Assess this cell for malaria.
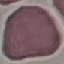

It is uninfected.

{
  "capture": "smartphone through the microscope eyepiece",
  "image_type": "automatically extracted cell patch, resized to 64 × 64 pixels",
  "preparation": "thin smear",
  "stain": "Giemsa"
}